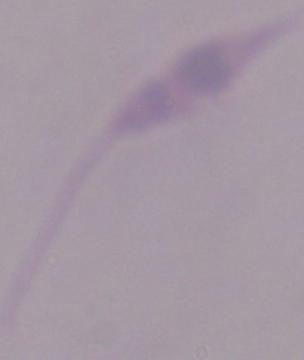
Summary:
  - Modality: photomicrograph
  - Identification: Leishmania
  - Magnification: 1000x